Locate every blood parasite and identify its species.
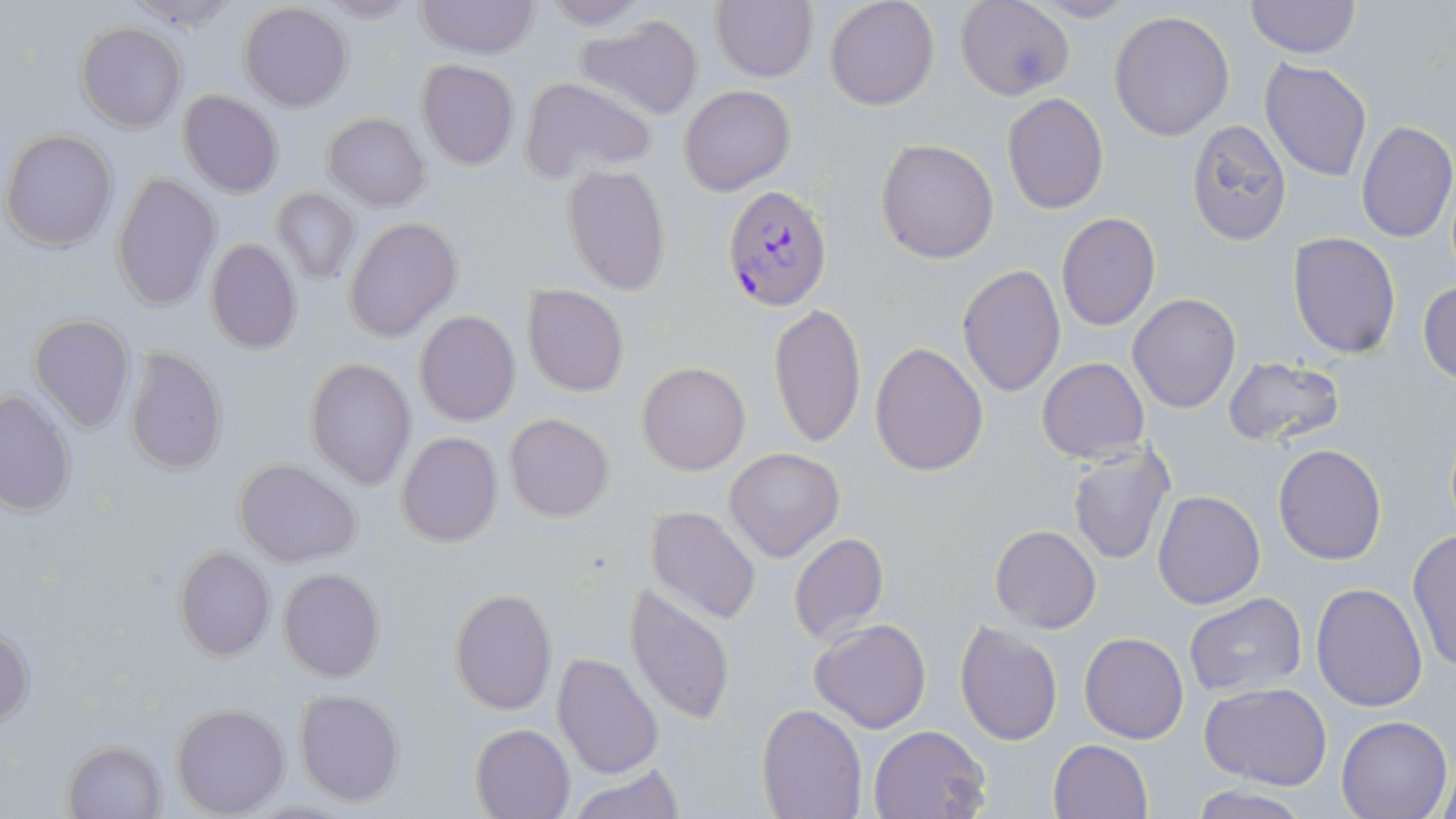

Approximate bounding boxes as (x1,y1)-(x2,y2) corner pairs in pixels.
Plasmodium falciparum-infected red blood cells: (724,186)-(832,312).
No Plasmodium ovale, Plasmodium malariae, Plasmodium vivax, Babesia divergens, or Trypanosoma brucei observed.

slide-level diagnosis = Plasmodium falciparum
magnification = 1000x
uninfected red blood cell locations = approximate bounding boxes as (x1,y1)-(x2,y2) corner pairs in pixels: (414,0)-(541,59), (535,0)-(655,30), (710,0)-(818,84), (824,0)-(940,111), (954,0)-(1075,104), (1019,1)-(1141,24), (1244,1)-(1362,58), (238,3)-(352,113), (1108,9)-(1236,141), (576,15)-(703,118), (75,22)-(188,133), (1259,58)-(1372,182), (415,60)-(520,171), (518,76)-(658,183), (679,85)-(796,196), (179,89)-(283,197), (1001,91)-(1110,215), (323,112)-(431,211), (1187,119)-(1291,247), (1356,121)-(1456,243), (2,129)-(117,252), (876,138)-(1001,264), (561,165)-(673,295), (113,173)-(220,310), (272,188)-(361,286), (1055,212)-(1162,330), (343,217)-(462,342), (1287,231)-(1401,360), (205,238)-(304,355), (956,265)-(1066,396), (1419,281)-(1456,384), (522,284)-(630,397), (1128,293)-(1241,413), (768,301)-(867,448), (413,311)-(520,426), (28,315)-(135,435), (869,342)-(988,476), (122,347)-(227,477), (1222,355)-(1346,448), (305,358)-(417,490), (1037,358)-(1149,462), (637,361)-(749,475), (0,389)-(75,517), (504,413)-(615,522), (396,432)-(503,547), (1065,443)-(1175,566), (1273,443)-(1387,566), (724,448)-(846,563), (233,458)-(362,568), (1153,490)-(1264,608), (646,505)-(761,626), (990,524)-(1102,632), (1408,527)-(1456,672), (788,532)-(888,645), (172,545)-(274,662), (278,568)-(385,683), (624,583)-(736,728), (1311,583)-(1428,712), (449,587)-(558,716), (1183,594)-(1308,701), (808,619)-(931,734), (953,620)-(1063,747), (1,625)-(34,728), (1079,633)-(1187,743), (552,653)-(664,776), (1200,683)-(1332,787), (293,689)-(406,807), (171,702)-(289,816), (757,702)-(866,818), (1335,715)-(1451,819), (471,722)-(576,818), (868,725)-(991,819), (1048,738)-(1153,819), (62,741)-(167,817), (570,765)-(688,817), (1187,786)-(1312,818)
field of view = single
image size = 1456×819 pixels
modality = light microscopy
stain = May-Grünwald-Giemsa
preparation = thin blood film